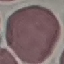
{
  "malaria_status": "uninfected",
  "image_type": "automatically extracted cell patch, resized to 64 × 64 pixels",
  "capture": "smartphone camera at the microscope eyepiece",
  "stain": "Giemsa",
  "preparation": "thin smear"
}